Outline every leukocyte.
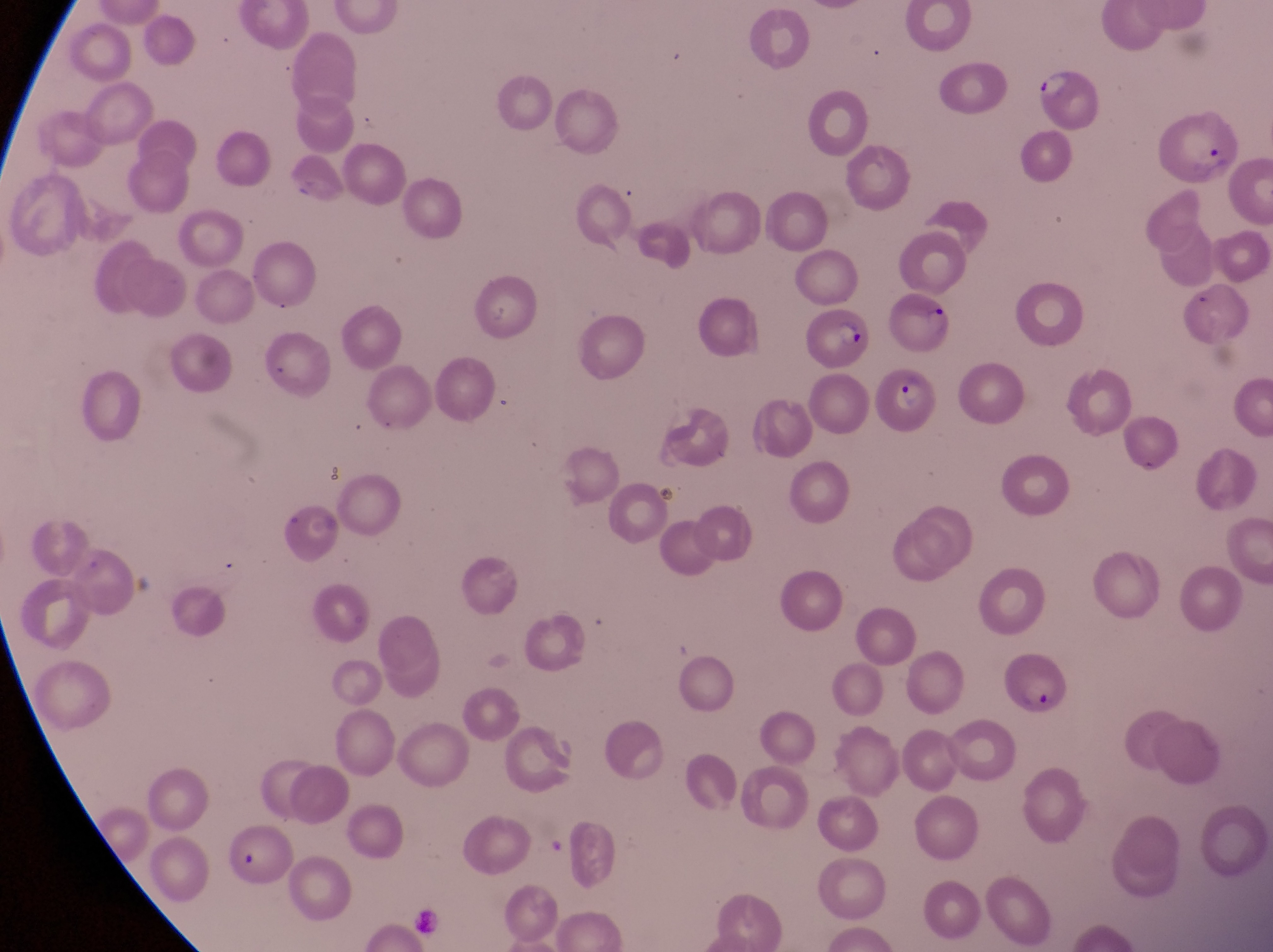
No leukocytes observed.

Approximate bounding boxes as (left, top, right, bottom) in pixels.
Summary:
  - Parasitised red blood cell locations: (1033, 65, 1102, 132), (1160, 104, 1238, 182), (801, 305, 871, 372), (869, 365, 941, 442), (999, 644, 1071, 724)
  - Preparation: thin blood film
  - Magnification: 1000x
  - Image size: 1273×952 pixels
  - Capture: smartphone photograph through the eyepiece of an Olympus CX-23 microscope
  - Field of view: single
  - Country: Uganda